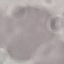
result = no malaria parasites seen
preparation = thin blood smear
capture = smartphone camera at the microscope eyepiece
stain = Giemsa
image type = automatically extracted cell patch, resized to 64 × 64 pixels